Name the parasite shown.
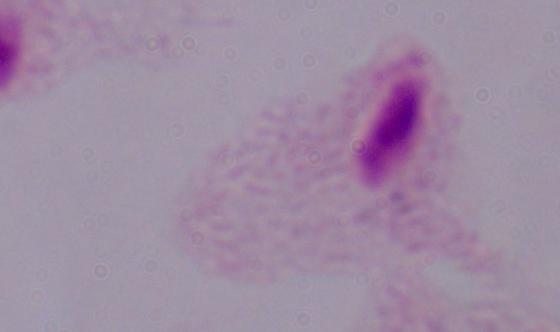

A trichomonad.

{
  "modality": "photomicrograph",
  "magnification": "1000x"
}